Assess this cell for malaria.
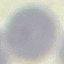
It is uninfected.

Summary:
  - Stain: Giemsa
  - Capture: smartphone camera at the microscope eyepiece
  - Preparation: thin blood film
  - Image type: automatically extracted cell patch, resized to 64 × 64 pixels